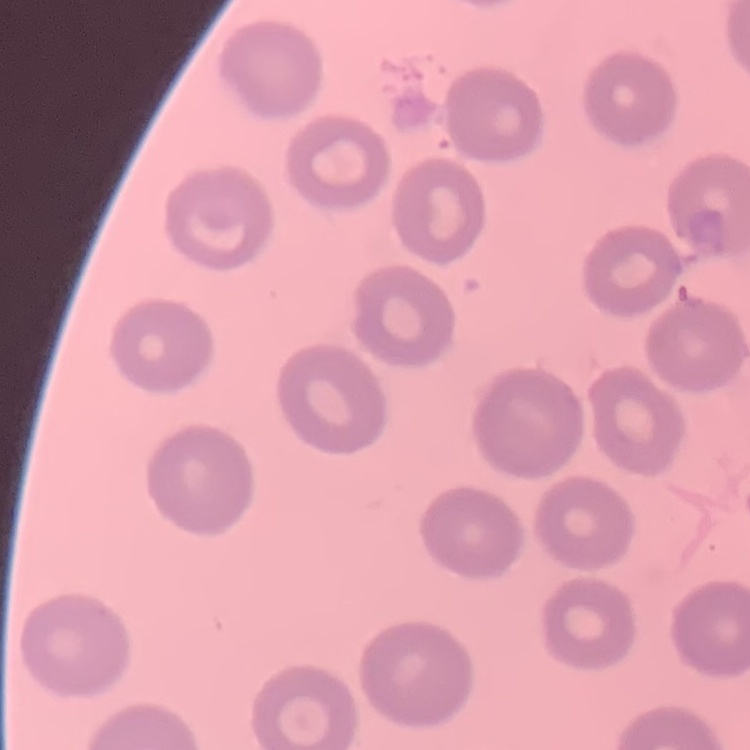
The erythrocytes exhibit no rouleaux formation. Stained with either Field's or Giemsa. One tile cut from a larger photomicrograph. Thin peripheral smear.